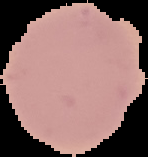
From a thin blood film. Image is 148×157 pixels. The area outside the segmented cell region is set to black. Result: no Plasmodium parasites seen.